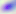

Summary:
  - Magnification: 400x
  - Identification: Toxoplasma gondii
  - Modality: micrograph